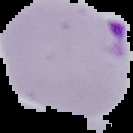

{
  "image_size": "133×133 pixels",
  "malaria_status": "parasitized",
  "preparation": "thin blood film",
  "image_type": "segmented cell region with the area outside set to black"
}